Outline each blood parasite and name the species.
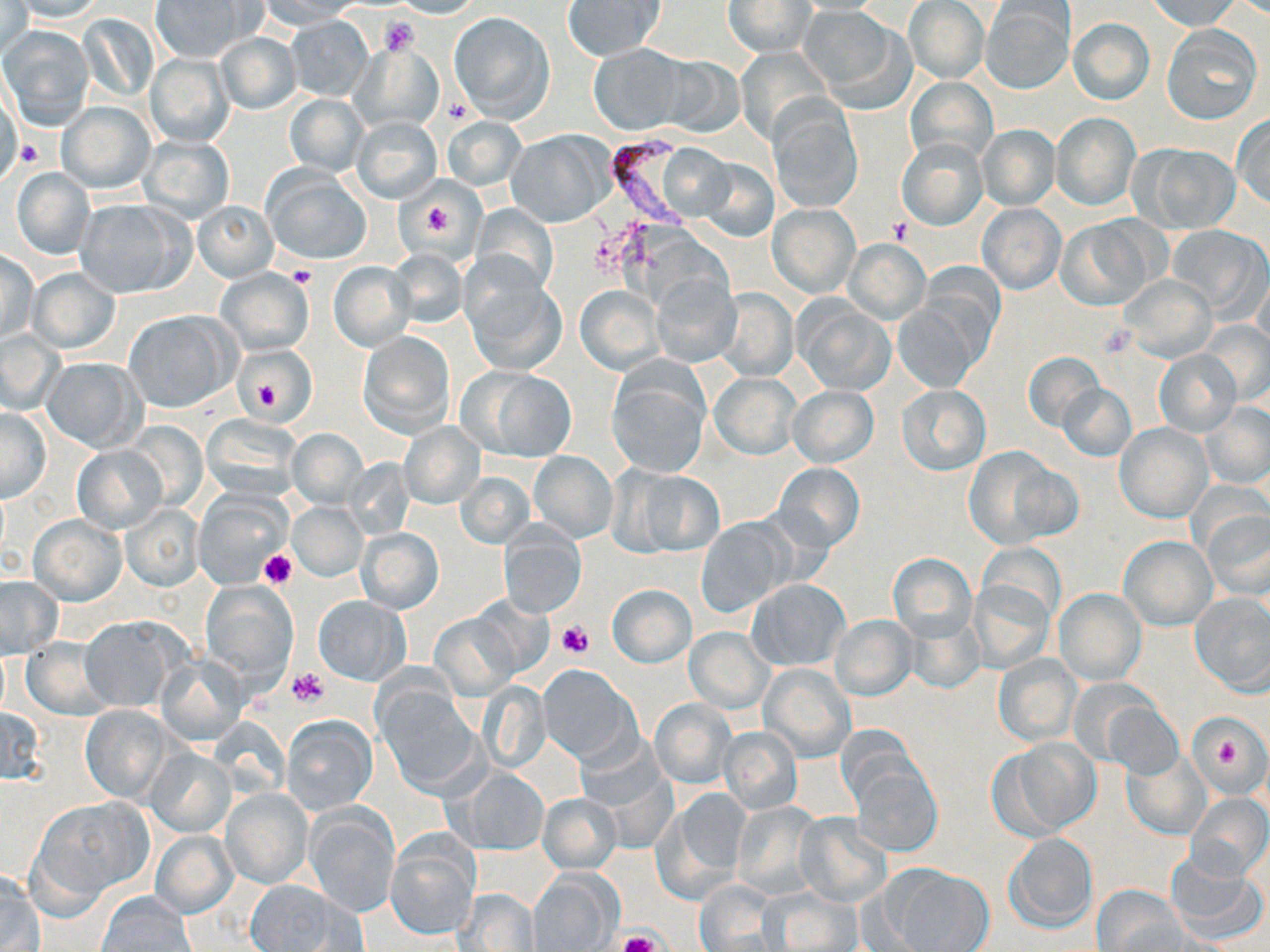

Approximate bounding boxes as (x1,y1)-(x2,y2) corner pairs in pixels.
Plasmodium falciparum-infected red blood cells: (608,132)-(688,233).
No Plasmodium ovale, Plasmodium malariae, Plasmodium vivax, Babesia divergens, or Trypanosoma brucei observed.

Platelet locations: (380,17)-(421,56), (16,140)-(42,169), (415,194)-(461,244), (889,218)-(913,242), (286,265)-(317,289), (1099,324)-(1137,358), (248,364)-(287,416), (258,548)-(295,589), (556,619)-(594,658), (288,668)-(329,709), (1215,738)-(1245,772), (616,931)-(661,952). Uninfected red blood cell locations: (7,0)-(108,22), (254,0)-(359,29), (389,0)-(485,18), (1145,0)-(1241,31), (151,1)-(249,61), (563,1)-(666,62), (723,1)-(814,58), (903,1)-(989,83), (980,2)-(1075,94), (0,4)-(33,57), (801,6)-(903,103), (449,11)-(555,122), (79,14)-(157,104), (286,17)-(373,99), (1068,18)-(1155,105), (1,26)-(94,129), (1161,26)-(1262,124), (215,32)-(301,114), (350,42)-(444,134), (587,44)-(689,135), (737,47)-(834,146), (145,52)-(235,148), (653,55)-(744,137), (904,76)-(997,167), (0,91)-(23,187), (284,93)-(369,177), (768,97)-(863,213), (57,101)-(155,192), (1052,112)-(1141,211), (1232,115)-(1270,209), (442,116)-(526,191), (352,117)-(442,202), (978,124)-(1059,209), (506,131)-(611,227), (138,136)-(235,223), (897,137)-(987,230), (1137,144)-(1240,232), (657,145)-(737,222), (698,157)-(779,241), (10,166)-(95,260), (263,169)-(371,264), (75,199)-(187,298), (194,201)-(277,281), (470,204)-(558,294), (978,204)-(1065,293), (769,205)-(859,297), (1056,218)-(1155,310), (1167,225)-(1268,318), (843,239)-(930,325), (387,248)-(467,328), (0,249)-(38,343), (328,262)-(413,351), (27,268)-(120,354), (216,268)-(313,355), (1253,270)-(1269,357), (463,274)-(567,376), (650,274)-(741,366), (1118,275)-(1216,361), (575,286)-(664,374), (715,290)-(797,381), (894,298)-(986,392), (796,301)-(894,395), (123,311)-(237,413), (1199,321)-(1270,405), (0,331)-(65,414), (358,332)-(454,437), (236,346)-(317,424), (1153,350)-(1241,438), (1024,352)-(1104,432), (41,357)-(145,453), (606,362)-(711,479), (466,367)-(577,461), (710,373)-(801,459), (1058,383)-(1136,461), (896,385)-(990,476), (787,386)-(878,467), (1199,403)-(1270,489), (1,407)-(50,501), (200,415)-(303,501), (123,421)-(207,511), (398,421)-(485,509), (1115,423)-(1212,523), (286,428)-(368,509), (73,445)-(165,532), (961,447)-(1072,548), (529,451)-(618,542), (343,458)-(416,538), (774,463)-(865,552), (624,467)-(726,557), (455,471)-(535,548), (193,491)-(289,588), (288,502)-(366,580), (119,503)-(205,592), (1201,507)-(1270,600), (29,514)-(126,606), (695,518)-(791,617), (498,523)-(586,618), (356,528)-(443,613), (1119,534)-(1216,630), (888,553)-(976,643), (0,576)-(63,658), (748,579)-(849,670), (968,579)-(1055,673), (201,582)-(297,684), (607,584)-(697,668), (1054,589)-(1146,684), (1190,593)-(1270,693), (312,594)-(410,685), (466,596)-(554,678), (429,614)-(519,698), (831,614)-(917,700), (79,617)-(181,712), (904,618)-(984,695), (684,627)-(773,714), (22,639)-(111,720), (994,654)-(1081,745), (156,655)-(248,745), (759,663)-(855,762), (538,665)-(638,765), (478,682)-(552,772), (380,686)-(481,794), (650,698)-(736,788), (1102,701)-(1183,780), (80,705)-(173,804), (0,706)-(46,785), (282,715)-(377,814), (1187,715)-(1267,797), (717,726)-(802,816), (576,735)-(671,822), (998,737)-(1101,837), (145,748)-(237,836), (1122,752)-(1209,839), (849,759)-(941,858), (457,770)-(549,855), (663,787)-(752,897), (222,788)-(311,888), (538,793)-(622,874), (1186,793)-(1269,881), (32,796)-(153,908), (733,800)-(826,898), (305,805)-(400,918), (794,814)-(892,907), (151,830)-(237,917), (1003,833)-(1099,934), (387,834)-(479,940), (1164,854)-(1267,947), (886,866)-(993,951), (528,870)-(620,951), (0,871)-(41,952), (244,881)-(363,951), (694,882)-(782,952), (1092,885)-(1182,951), (455,889)-(540,951), (763,890)-(860,951), (97,891)-(196,952). Slide-level diagnosis: Plasmodium falciparum. 1000x magnification. Single field of view. Thin blood smear. May-Grünwald-Giemsa stain. Light microscopy. Image is 1270×952 pixels.